Describe the morphology of the erythrocytes.
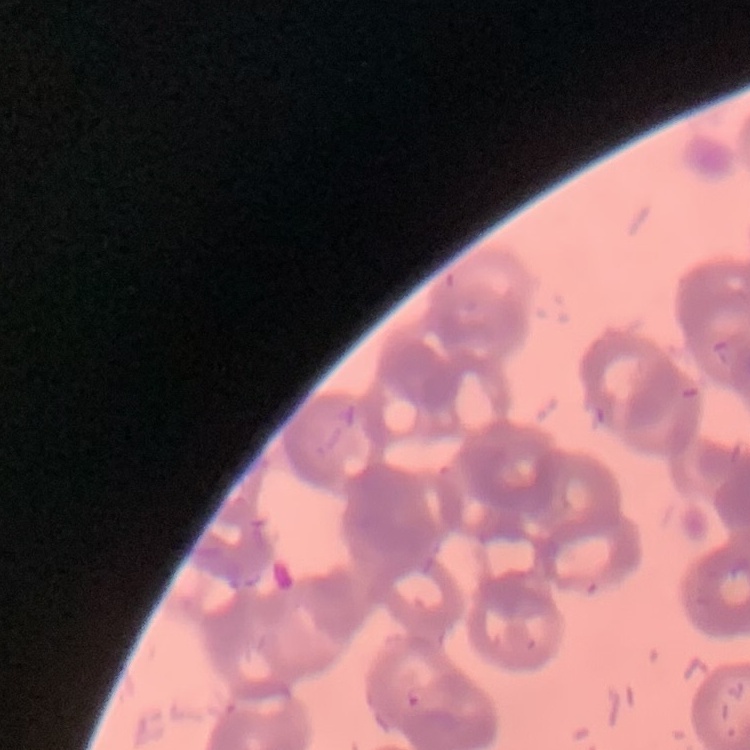
Rouleaux formation.

{
  "stain": "Field's or Giemsa",
  "preparation": "thin peripheral smear",
  "image_type": "square crop of a larger photomicrograph"
}